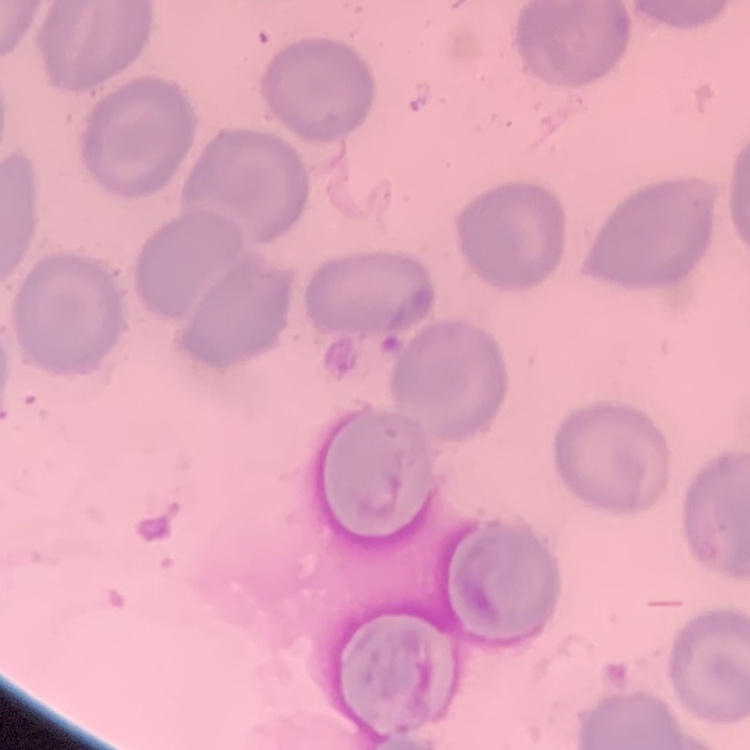 The red blood cells show no rouleaux formation. Thin blood smear. Square crop of a larger photomicrograph. Field's or Giemsa stain.